Classify this cell by malaria status.
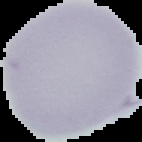
It is uninfected.

image size = 142×142 pixels
image type = cell region segmented out of the field of view; surrounding area masked to black
preparation = thin blood film